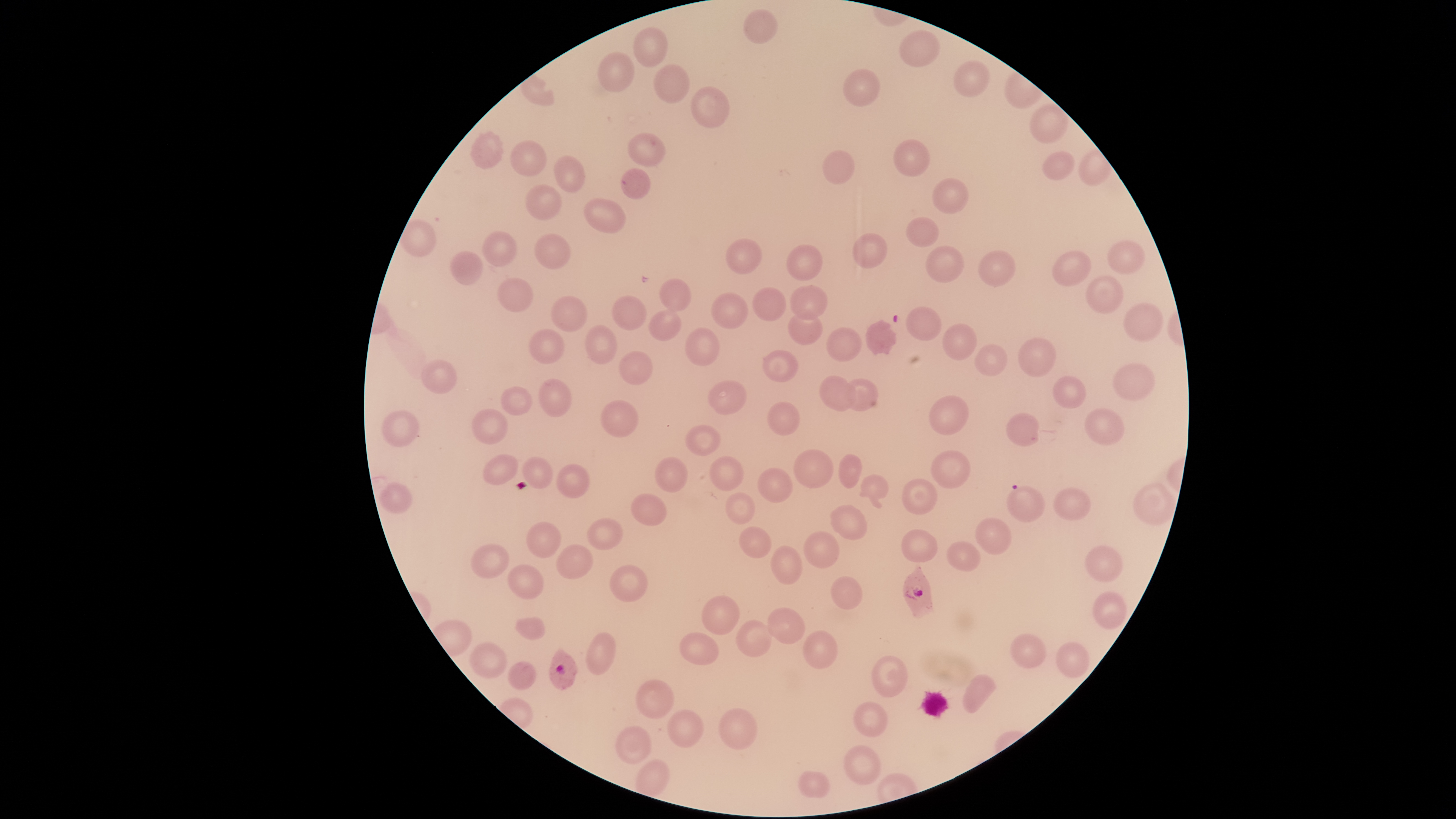
Approximate bounding boxes as [left, top, right, bottom] in pixels. Uninfected red blood cells: [744, 9, 777, 43], [633, 27, 668, 67], [900, 30, 940, 67], [599, 52, 633, 92], [954, 61, 990, 97], [654, 64, 689, 103], [843, 69, 880, 106], [691, 86, 729, 128], [1030, 104, 1068, 143], [471, 131, 504, 169], [628, 133, 665, 166], [894, 139, 929, 177], [510, 140, 546, 176], [822, 150, 855, 184], [1079, 150, 1113, 186], [1042, 152, 1075, 180], [554, 155, 585, 192], [622, 168, 650, 199], [932, 177, 968, 214], [526, 184, 562, 219], [584, 199, 626, 233], [906, 216, 939, 247], [401, 219, 436, 257], [482, 231, 517, 266], [853, 233, 887, 268], [535, 234, 571, 269], [726, 239, 762, 274], [1107, 240, 1144, 274], [787, 244, 823, 280], [926, 246, 965, 283], [979, 250, 1015, 287], [1053, 250, 1091, 287], [450, 251, 482, 285], [1086, 275, 1123, 314], [497, 277, 533, 312], [660, 278, 691, 310], [790, 285, 828, 319], [753, 287, 786, 321], [711, 293, 748, 329], [612, 295, 646, 330], [551, 296, 587, 331], [1124, 302, 1164, 341], [906, 306, 942, 341], [649, 309, 681, 341], [788, 311, 823, 345], [866, 320, 897, 356], [942, 323, 976, 361], [585, 325, 617, 364], [826, 327, 861, 362], [529, 328, 564, 365], [686, 328, 719, 366], [1018, 338, 1056, 377], [975, 344, 1007, 376], [763, 349, 799, 382], [619, 350, 653, 385], [422, 360, 457, 393], [1113, 363, 1155, 400], [819, 375, 856, 411], [1053, 376, 1085, 408], [539, 378, 571, 417], [845, 378, 879, 411], [708, 380, 747, 414], [501, 386, 532, 415], [929, 396, 969, 436], [601, 400, 638, 437], [767, 401, 800, 436], [1085, 408, 1125, 445], [473, 409, 508, 444], [383, 411, 419, 447], [1006, 413, 1039, 446], [686, 425, 720, 456], [794, 449, 833, 488], [931, 450, 970, 489], [484, 454, 517, 484], [839, 454, 862, 488], [709, 456, 743, 491], [523, 457, 552, 489], [655, 457, 687, 492], [557, 464, 590, 498], [757, 467, 792, 503], [860, 474, 889, 508], [902, 479, 937, 515], [379, 482, 412, 514], [1134, 483, 1176, 525], [1053, 487, 1091, 520], [726, 492, 754, 524], [631, 494, 666, 525], [830, 505, 867, 540], [975, 517, 1012, 554], [587, 518, 622, 550], [527, 522, 560, 558], [739, 526, 771, 558], [902, 529, 938, 563], [803, 530, 839, 568], [947, 541, 981, 571], [471, 544, 509, 578], [556, 545, 592, 578], [1085, 545, 1122, 582], [771, 546, 802, 584], [508, 564, 543, 599], [610, 565, 647, 602], [830, 576, 863, 609], [1092, 590, 1126, 629], [701, 595, 740, 635], [767, 607, 805, 644], [515, 616, 545, 640], [736, 620, 771, 657], [803, 630, 837, 668], [586, 632, 616, 674], [679, 632, 718, 665], [1010, 633, 1047, 668], [1056, 641, 1089, 678], [469, 642, 507, 678], [872, 655, 908, 697], [508, 661, 537, 690], [963, 674, 996, 713], [635, 679, 674, 719], [854, 702, 887, 737], [719, 708, 758, 750], [668, 709, 704, 748], [615, 726, 651, 764], [844, 745, 881, 785], [635, 759, 669, 797], [798, 771, 830, 798]. Parasitized red blood cells: [1007, 484, 1045, 522], [903, 566, 933, 618], [549, 649, 578, 691]. Thin smear of blood. Giemsa stain. Circular visible region. Image is 1456×819 pixels. Species: Plasmodium falciparum. Single field of view. Smartphone photograph through the microscope eyepiece. Presence: malaria parasites detected.